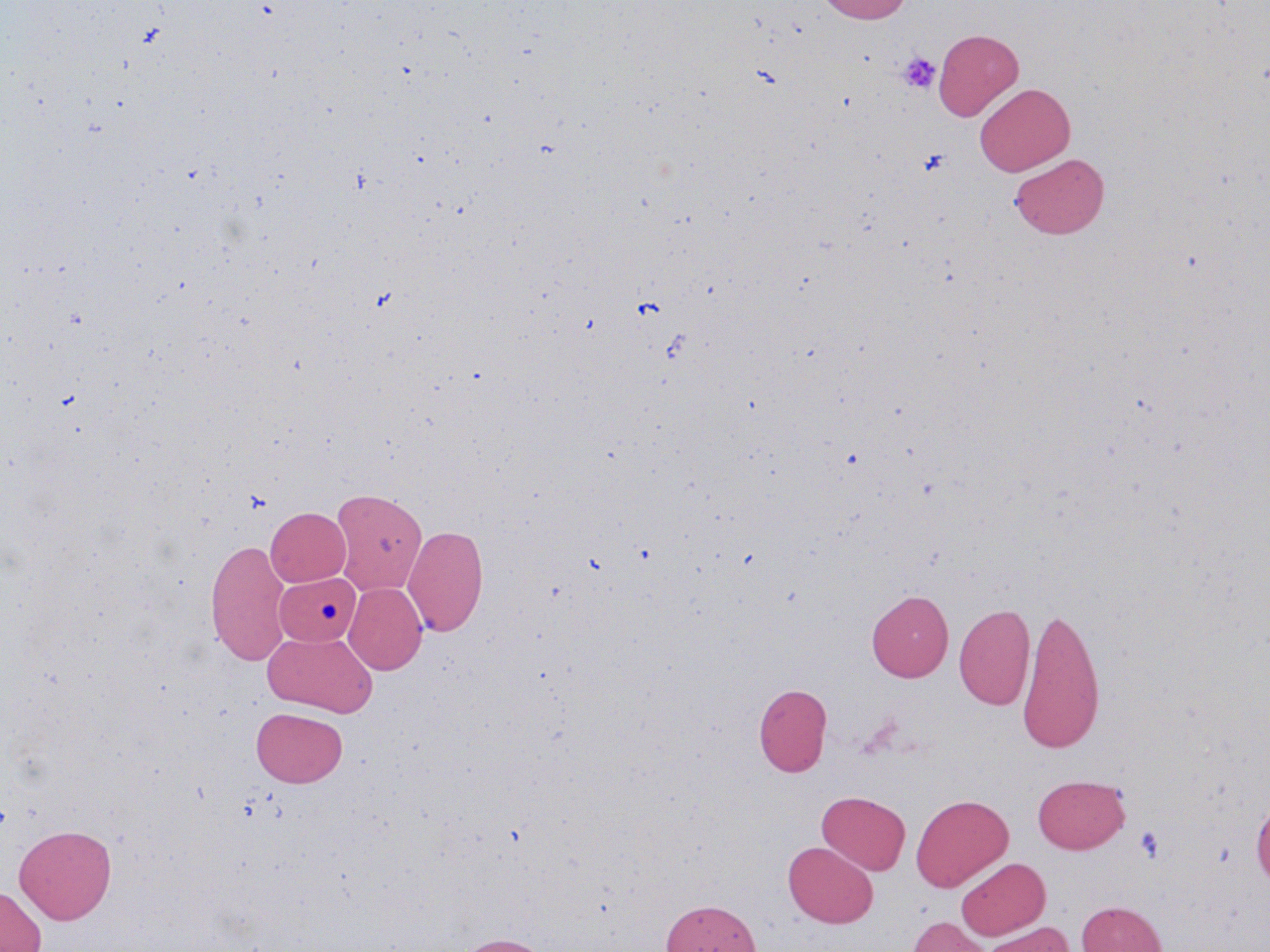
{
  "slide_level_diagnosis": "negative for blood parasites",
  "preparation": "thin blood smear",
  "modality": "light microscopy",
  "image_size": "1270×952 pixels",
  "platelet_locations": "approximate bounding boxes as [x1, y1, x2, y2] in pixels: [898, 51, 941, 93], [918, 148, 951, 176], [1135, 825, 1164, 861]",
  "uninfected_red_blood_cell_locations": "approximate bounding boxes as [x1, y1, x2, y2] in pixels: [815, 0, 913, 23], [933, 28, 1023, 122], [975, 83, 1075, 176], [1009, 152, 1109, 238], [330, 488, 427, 595], [265, 507, 351, 586], [403, 523, 488, 637], [205, 538, 291, 666], [277, 574, 362, 647], [344, 582, 427, 675], [867, 590, 953, 682], [954, 602, 1035, 711], [1017, 603, 1106, 753], [262, 630, 378, 716], [754, 683, 832, 777], [251, 707, 347, 787], [1032, 774, 1130, 853], [817, 791, 910, 875], [911, 794, 1013, 892], [1251, 794, 1270, 888], [15, 824, 116, 923], [783, 841, 878, 928], [956, 857, 1050, 940], [0, 886, 47, 952], [661, 899, 760, 952], [1076, 900, 1167, 952], [908, 916, 993, 952], [981, 922, 1074, 952], [451, 933, 552, 952]",
  "magnification": "1000x",
  "field_of_view": "single",
  "stain": "May-Grünwald-Giemsa"
}